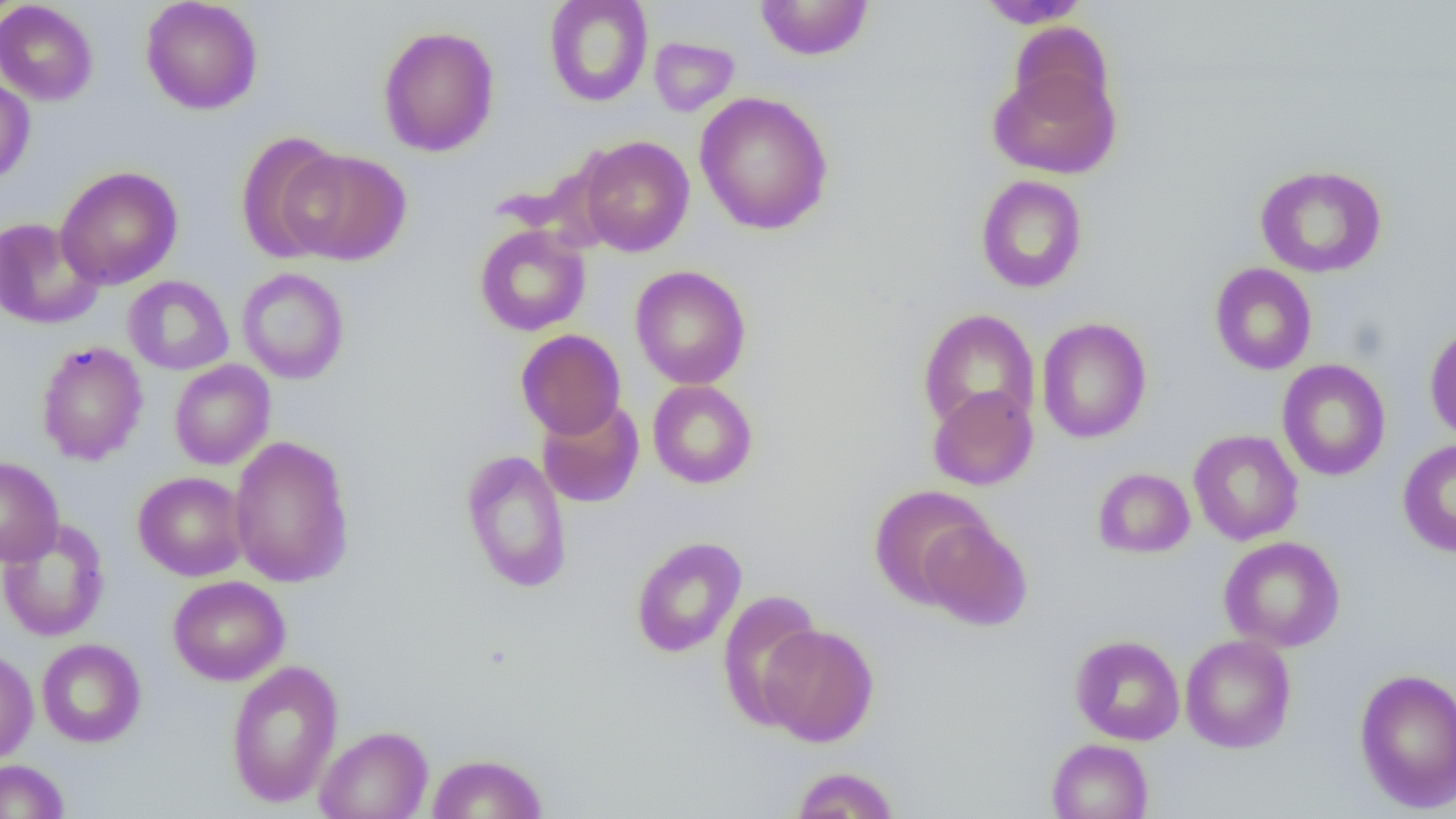

Summary:
  - Coordinate format: approximate bounding boxes as named x1/y1/x2/y2 corners in pixels
  - Uninfected red blood cell locations: (x1=140, y1=0, x2=263, y2=115), (x1=543, y1=0, x2=653, y2=107), (x1=756, y1=0, x2=873, y2=60), (x1=976, y1=0, x2=1092, y2=28), (x1=0, y1=1, x2=99, y2=105), (x1=1009, y1=22, x2=1114, y2=119), (x1=377, y1=25, x2=500, y2=157), (x1=648, y1=36, x2=740, y2=117), (x1=988, y1=64, x2=1120, y2=179), (x1=0, y1=75, x2=35, y2=185), (x1=694, y1=91, x2=834, y2=236), (x1=235, y1=131, x2=347, y2=264), (x1=577, y1=135, x2=695, y2=257), (x1=280, y1=149, x2=411, y2=265), (x1=1255, y1=164, x2=1387, y2=278), (x1=55, y1=166, x2=183, y2=290), (x1=975, y1=174, x2=1088, y2=293), (x1=0, y1=216, x2=105, y2=330), (x1=474, y1=224, x2=590, y2=336), (x1=1210, y1=263, x2=1317, y2=375), (x1=630, y1=265, x2=751, y2=389), (x1=236, y1=267, x2=350, y2=384), (x1=123, y1=275, x2=233, y2=375), (x1=918, y1=308, x2=1040, y2=433), (x1=1036, y1=317, x2=1152, y2=444), (x1=1424, y1=321, x2=1456, y2=443), (x1=516, y1=329, x2=626, y2=440), (x1=35, y1=341, x2=148, y2=465), (x1=1277, y1=359, x2=1391, y2=481), (x1=169, y1=360, x2=275, y2=470), (x1=647, y1=380, x2=758, y2=489), (x1=927, y1=384, x2=1038, y2=491), (x1=536, y1=399, x2=645, y2=508), (x1=1188, y1=430, x2=1303, y2=545), (x1=229, y1=435, x2=355, y2=588), (x1=1397, y1=439, x2=1456, y2=557), (x1=460, y1=448, x2=573, y2=594), (x1=0, y1=457, x2=64, y2=567), (x1=1093, y1=460, x2=1303, y2=550), (x1=1093, y1=467, x2=1195, y2=558), (x1=133, y1=471, x2=249, y2=581), (x1=869, y1=485, x2=994, y2=607), (x1=0, y1=518, x2=110, y2=642), (x1=918, y1=518, x2=1032, y2=631), (x1=630, y1=536, x2=747, y2=658), (x1=1218, y1=536, x2=1346, y2=652), (x1=168, y1=575, x2=290, y2=685), (x1=716, y1=590, x2=825, y2=727), (x1=757, y1=623, x2=880, y2=746), (x1=1070, y1=634, x2=1185, y2=745), (x1=1180, y1=634, x2=1296, y2=753), (x1=36, y1=638, x2=146, y2=747), (x1=0, y1=648, x2=39, y2=765), (x1=226, y1=660, x2=343, y2=807), (x1=1353, y1=668, x2=1456, y2=812), (x1=315, y1=726, x2=433, y2=819), (x1=1046, y1=738, x2=1153, y2=819), (x1=428, y1=752, x2=547, y2=818), (x1=0, y1=759, x2=70, y2=819), (x1=790, y1=766, x2=900, y2=819)
  - Slide-level diagnosis: no evidence of blood parasites
  - Modality: optical microscopy
  - Preparation: thin blood film
  - Magnification: 1000x
  - Field of view: single
  - Image size: 1456×819 pixels